Assess this cell for malaria.
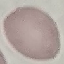
It is uninfected.

Summary:
  - Capture: smartphone camera at the microscope eyepiece
  - Stain: Giemsa
  - Image type: cell patch, automatically extracted from a larger field of view and resized to 64 × 64 pixels
  - Preparation: thin blood smear